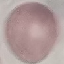
{
  "result": "no malaria parasites detected",
  "capture": "smartphone camera at the microscope eyepiece",
  "image_type": "automatically extracted cell patch, resized to 64 × 64 pixels",
  "preparation": "thin blood film",
  "stain": "Giemsa"
}